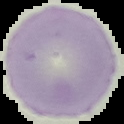 Image is 124×124 pixels. Result: no Plasmodium parasites detected. Segmented cell region on a black background. From a thin blood smear.